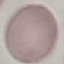

malaria_status: uninfected
preparation: thin smear
stain: Giemsa
capture: smartphone through the microscope eyepiece
image_type: automatically extracted cell patch, resized to 64 × 64 pixels